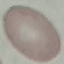
malaria_status: uninfected
image_type: automatically extracted cell patch, resized to 64 × 64 pixels
preparation: thin blood smear
capture: smartphone through the microscope eyepiece
stain: Giemsa